Locate every Plasmodium parasite.
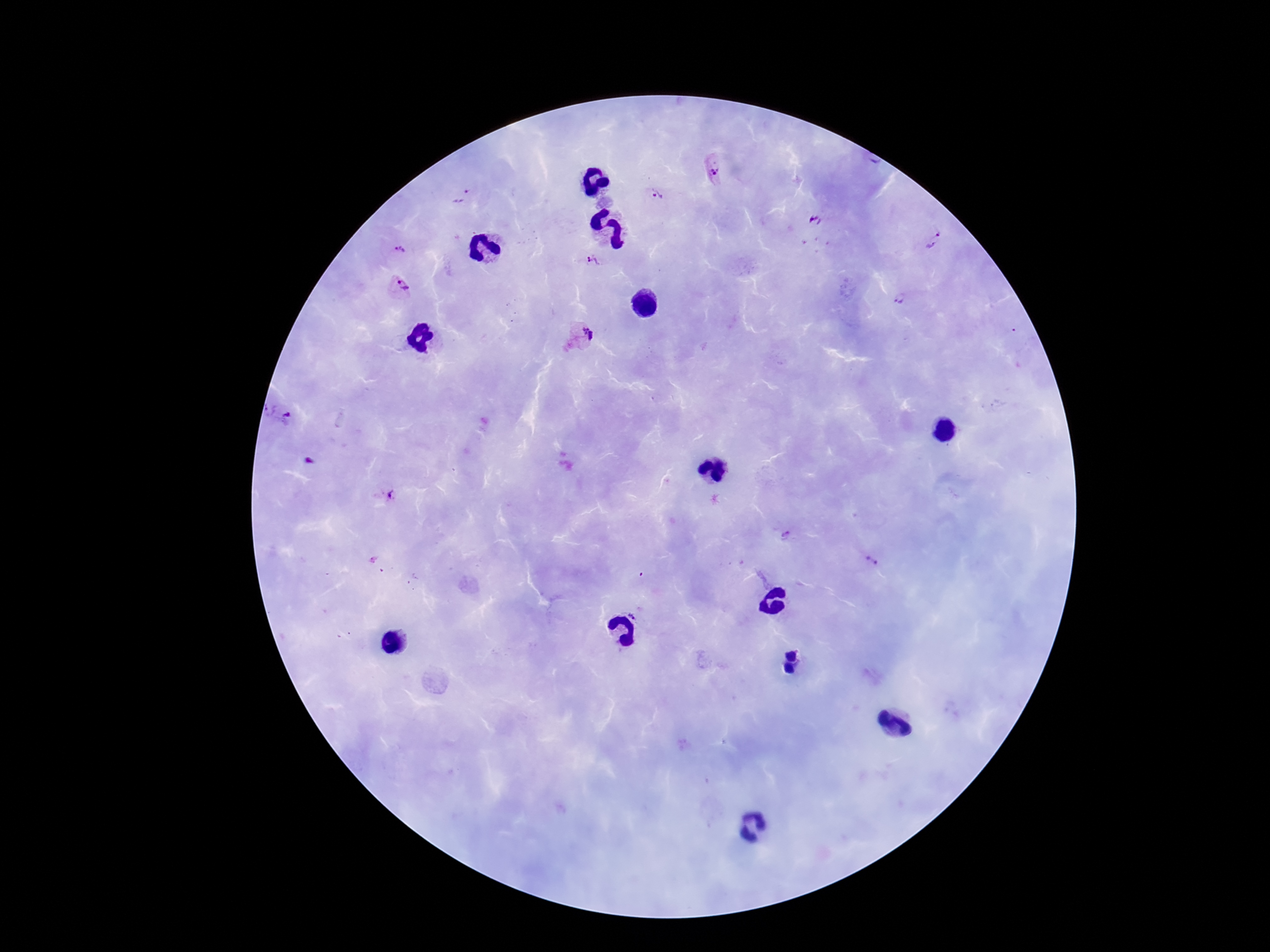

Approximate centers as {x, y} in pixels.
Plasmodium parasites: {711, 172}, {656, 195}, {462, 196}, {815, 221}, {935, 241}, {401, 250}, {592, 262}, {402, 287}, {900, 300}, {588, 333}, {283, 416}, {388, 494}, {787, 537}, {871, 561}, {638, 609}.

Summary:
  - Magnification: 100x
  - Image size: 1270×952 pixels
  - Patient malaria status: positive
  - Field of view: one from this slide
  - Capture: smartphone camera through the microscope eyepiece
  - Preparation: thick blood smear
  - Stain: Giemsa